Identify the preparation type.
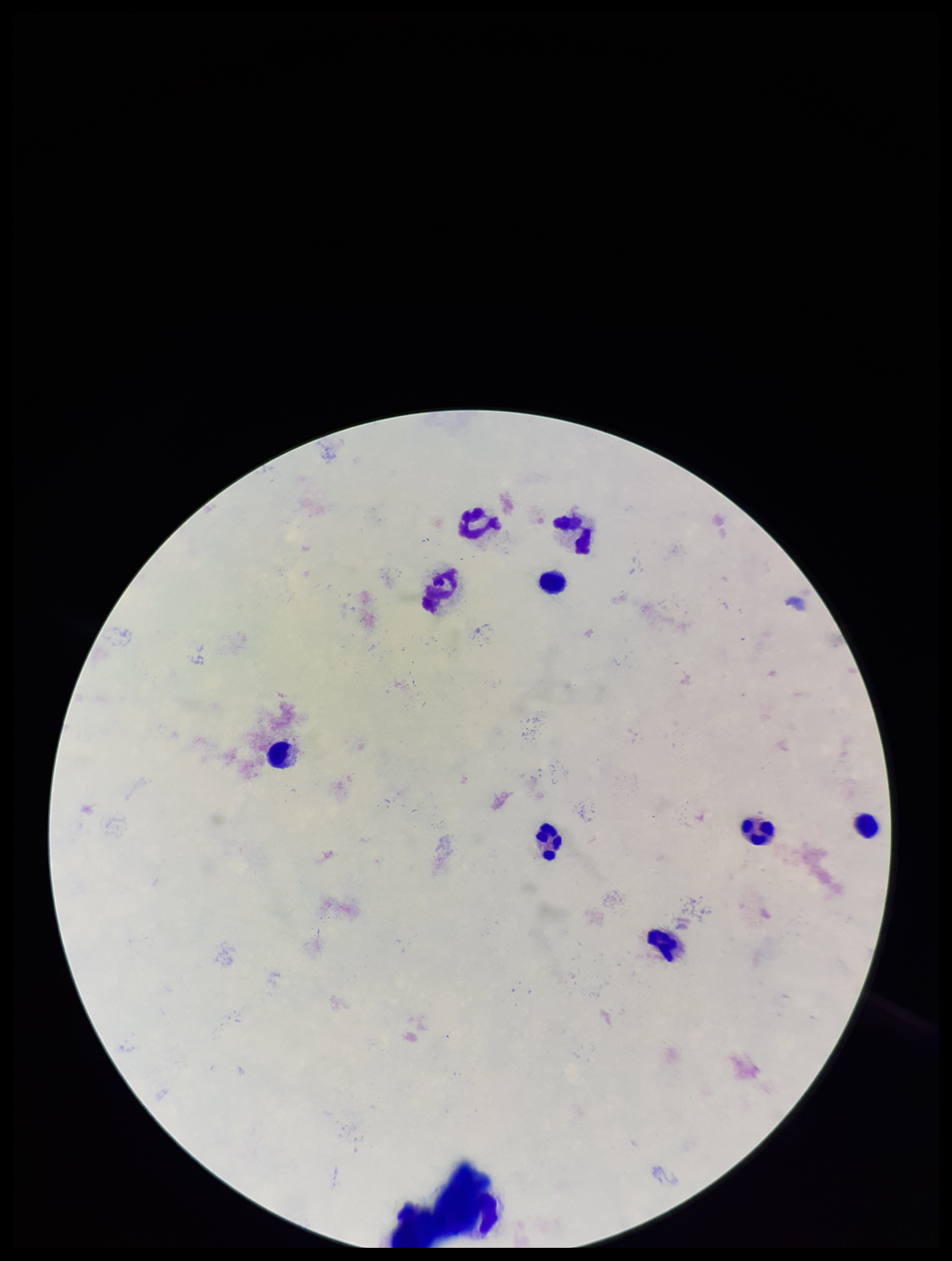
Thick.

Photographed through the microscope eyepiece with a smartphone camera. Leukocyte count: 9. Plasmodium parasites: none detected. Patient malaria status: negative. Image is 952×1261 pixels. Single field of view. Stained with Giemsa. Parasite count: 0.